Identify the parasite.
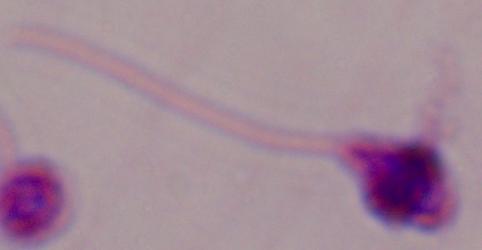

Leishmania.

1000x magnification. Photomicrograph.